Identify the parasite.
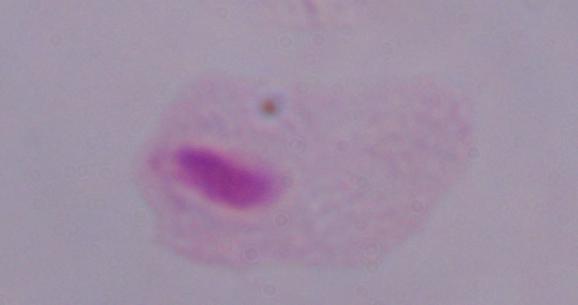
A trichomonad.

{
  "modality": "micrograph",
  "magnification": "1000x"
}